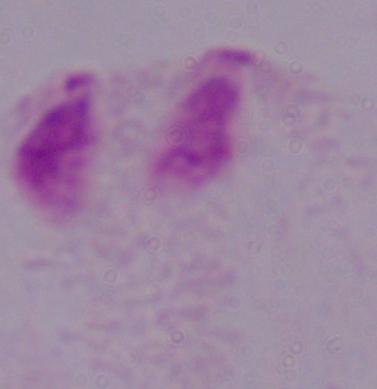

Photomicrograph. A trichomonad is shown. 1000x magnification.